Report the malaria status of this cell.
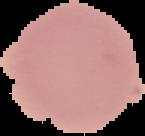

Uninfected.

Image is 145×136 pixels. Segmented cell region on a black background. From a thin blood smear.